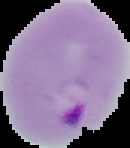
image_type: segmented cell region on a black background
preparation: thin blood film
image_size: 130×148 pixels
malaria_status: parasitized